Classify this cell by malaria status.
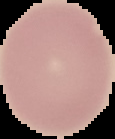

It is uninfected.

Cell region segmented out of the field of view; the surrounding area is masked to black. Image is 115×139 pixels. From a thin blood smear.